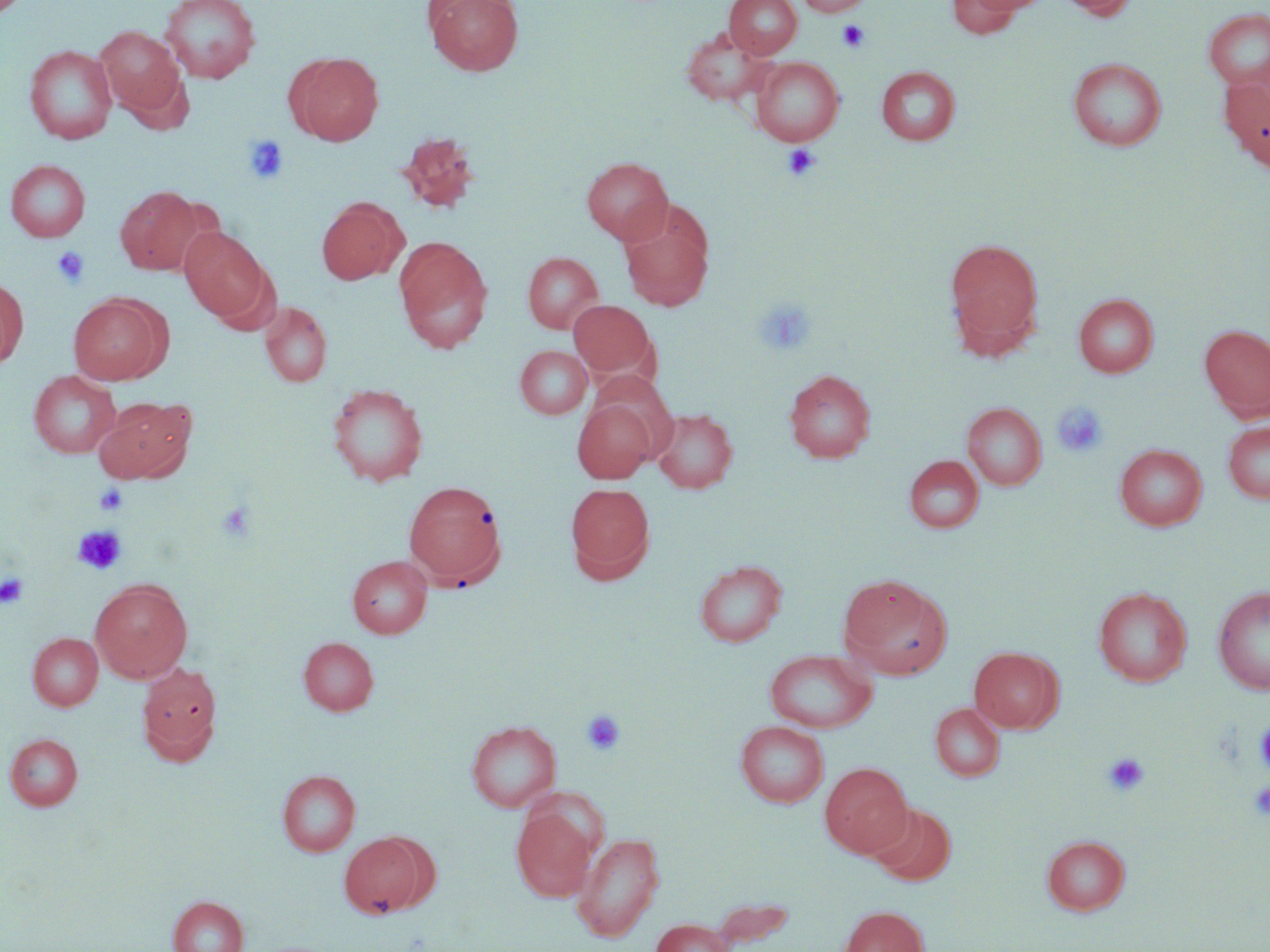
Summary:
  - Coordinate format: approximate bounding boxes as named x1/y1/x2/y2 corners in pixels
  - Uninfected red blood cell locations: (x1=159, y1=0, x2=261, y2=83), (x1=425, y1=0, x2=524, y2=76), (x1=724, y1=0, x2=802, y2=58), (x1=795, y1=0, x2=871, y2=16), (x1=1057, y1=0, x2=1139, y2=20), (x1=946, y1=1, x2=1028, y2=38), (x1=1203, y1=8, x2=1270, y2=91), (x1=95, y1=25, x2=187, y2=120), (x1=682, y1=27, x2=770, y2=105), (x1=24, y1=44, x2=117, y2=144), (x1=289, y1=52, x2=384, y2=146), (x1=750, y1=57, x2=844, y2=146), (x1=1067, y1=57, x2=1168, y2=151), (x1=876, y1=66, x2=961, y2=146), (x1=1220, y1=76, x2=1270, y2=170), (x1=396, y1=132, x2=480, y2=213), (x1=581, y1=157, x2=673, y2=244), (x1=5, y1=159, x2=91, y2=242), (x1=115, y1=186, x2=205, y2=274), (x1=316, y1=197, x2=407, y2=285), (x1=619, y1=206, x2=714, y2=311), (x1=179, y1=226, x2=271, y2=322), (x1=393, y1=236, x2=493, y2=353), (x1=944, y1=237, x2=1045, y2=353), (x1=523, y1=252, x2=604, y2=334), (x1=0, y1=277, x2=29, y2=368), (x1=68, y1=293, x2=168, y2=384), (x1=1073, y1=294, x2=1159, y2=377), (x1=568, y1=300, x2=657, y2=380), (x1=260, y1=302, x2=331, y2=387), (x1=1200, y1=325, x2=1270, y2=419), (x1=515, y1=346, x2=592, y2=419), (x1=783, y1=369, x2=876, y2=463), (x1=28, y1=370, x2=122, y2=459), (x1=327, y1=382, x2=428, y2=486), (x1=95, y1=396, x2=196, y2=483), (x1=572, y1=398, x2=657, y2=483), (x1=962, y1=402, x2=1047, y2=491), (x1=651, y1=407, x2=738, y2=494), (x1=1222, y1=420, x2=1270, y2=505), (x1=1115, y1=444, x2=1207, y2=531), (x1=904, y1=455, x2=984, y2=533), (x1=403, y1=480, x2=508, y2=588), (x1=565, y1=482, x2=655, y2=582), (x1=347, y1=555, x2=432, y2=638), (x1=693, y1=559, x2=788, y2=647), (x1=838, y1=574, x2=952, y2=678), (x1=89, y1=578, x2=193, y2=683), (x1=1213, y1=585, x2=1270, y2=695), (x1=1093, y1=586, x2=1192, y2=687), (x1=28, y1=632, x2=103, y2=711), (x1=298, y1=636, x2=378, y2=715), (x1=968, y1=646, x2=1063, y2=733), (x1=764, y1=649, x2=877, y2=733), (x1=137, y1=663, x2=223, y2=765), (x1=930, y1=703, x2=1004, y2=782), (x1=466, y1=720, x2=562, y2=813), (x1=735, y1=721, x2=829, y2=808), (x1=5, y1=733, x2=83, y2=810), (x1=820, y1=762, x2=913, y2=858), (x1=277, y1=770, x2=361, y2=857), (x1=868, y1=802, x2=957, y2=886), (x1=512, y1=809, x2=596, y2=901), (x1=339, y1=831, x2=434, y2=918), (x1=572, y1=832, x2=665, y2=941), (x1=1041, y1=834, x2=1130, y2=915), (x1=167, y1=896, x2=249, y2=952), (x1=838, y1=905, x2=930, y2=952), (x1=650, y1=918, x2=733, y2=952)
  - Platelet locations: (x1=837, y1=19, x2=871, y2=53), (x1=242, y1=134, x2=290, y2=185), (x1=782, y1=144, x2=821, y2=181), (x1=51, y1=246, x2=90, y2=288), (x1=754, y1=297, x2=817, y2=356), (x1=1051, y1=402, x2=1109, y2=458), (x1=94, y1=483, x2=129, y2=516), (x1=216, y1=501, x2=256, y2=542), (x1=72, y1=525, x2=128, y2=574), (x1=0, y1=572, x2=29, y2=608), (x1=581, y1=708, x2=627, y2=756), (x1=1256, y1=720, x2=1270, y2=774), (x1=1103, y1=752, x2=1150, y2=796), (x1=1249, y1=780, x2=1270, y2=821)
  - Slide-level diagnosis: negative for blood parasites
  - Modality: optical microscopy
  - Image size: 1270×952 pixels
  - Field of view: single
  - Preparation: thin blood smear
  - Stain: May-Grünwald-Giemsa
  - Magnification: 1000x